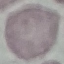

result = no malaria parasites detected
capture = smartphone camera at the microscope eyepiece
stain = Giemsa
preparation = thin smear
image type = cell patch, automatically extracted from a larger field of view and resized to 64 × 64 pixels